Outline each blood parasite and name the species.
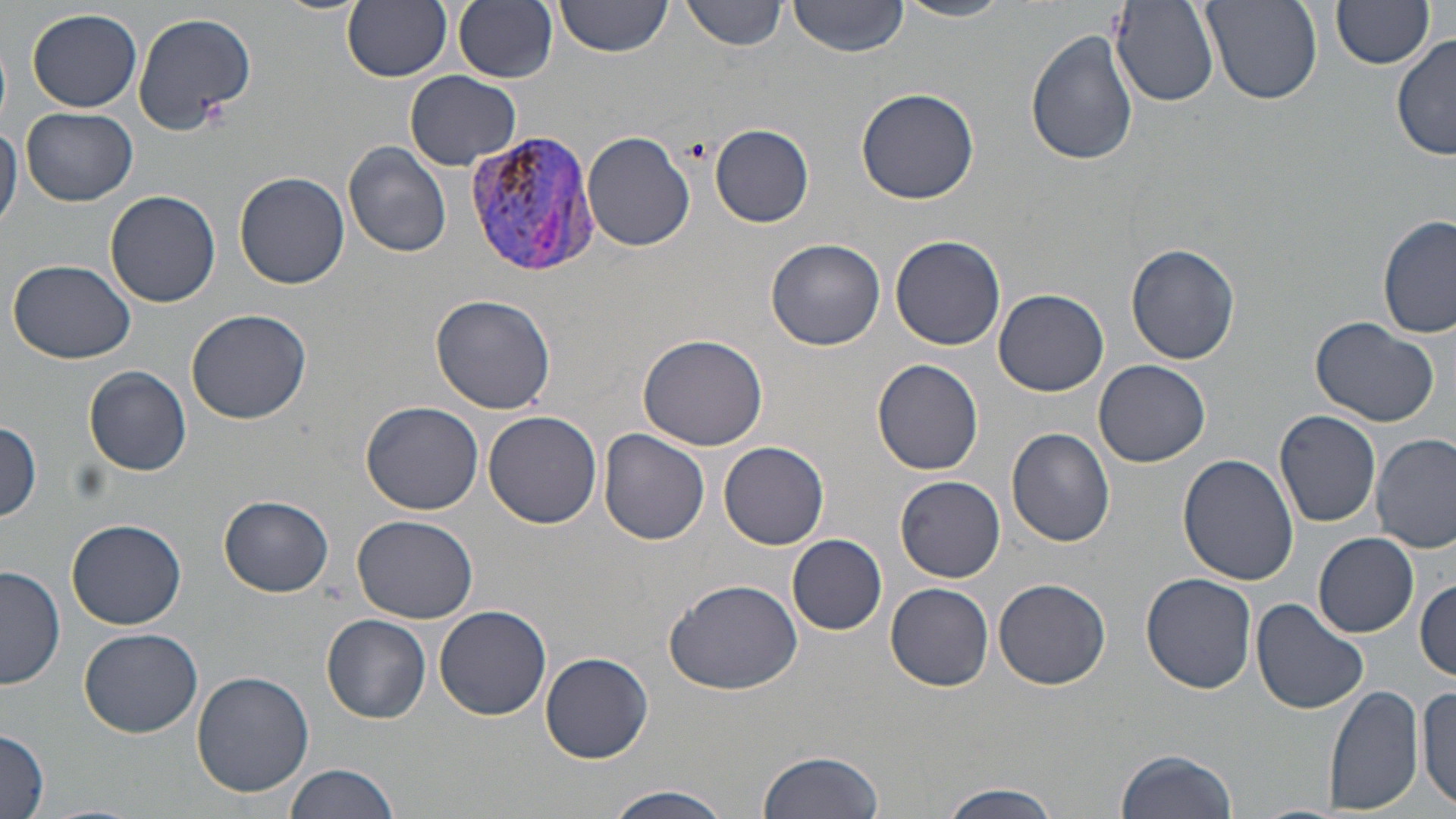

Approximate bounding boxes as (x1,y1)-(x2,y2) corner pairs in pixels.
Plasmodium vivax-infected red blood cells: (465,126)-(598,279).
No Plasmodium falciparum, Plasmodium ovale, Plasmodium malariae, Babesia divergens, or Trypanosoma brucei observed.

Uninfected red blood cell locations: (273,0)-(363,15), (342,0)-(453,82), (438,0)-(547,163), (453,0)-(559,82), (553,0)-(671,61), (682,0)-(790,52), (787,0)-(911,56), (896,0)-(1012,23), (1113,1)-(1221,107), (1201,1)-(1322,104), (1331,1)-(1434,70), (28,8)-(143,111), (130,9)-(259,136), (1026,29)-(1138,167), (1391,33)-(1455,160), (0,35)-(11,128), (405,72)-(524,172), (855,86)-(980,204), (21,108)-(141,206), (0,119)-(21,235), (711,124)-(814,228), (583,133)-(694,252), (343,142)-(453,258), (234,170)-(350,289), (105,190)-(221,308), (1377,215)-(1454,337), (890,236)-(1007,352), (766,238)-(885,350), (1127,246)-(1240,365), (8,258)-(137,365), (994,288)-(1109,396), (430,293)-(556,414), (186,309)-(312,424), (1309,317)-(1439,427), (637,333)-(769,451), (872,358)-(986,475), (1094,360)-(1212,468), (85,366)-(192,476), (360,400)-(486,514), (482,409)-(603,530), (1273,410)-(1383,528), (0,421)-(44,523), (597,428)-(711,545), (1006,428)-(1117,548), (1371,431)-(1455,553), (719,441)-(830,549), (1180,453)-(1298,585), (895,475)-(1006,583), (219,494)-(333,597), (352,514)-(476,623), (68,519)-(186,630), (787,533)-(887,635), (1314,533)-(1420,637), (0,563)-(66,692), (1141,572)-(1258,694), (665,575)-(805,696), (994,577)-(1111,690), (1415,579)-(1455,681), (886,582)-(994,691), (1251,598)-(1370,715), (434,606)-(552,721), (321,615)-(431,722), (79,627)-(204,737), (540,653)-(653,762), (192,670)-(314,797), (1324,684)-(1424,815), (1417,685)-(1455,813), (0,729)-(50,818), (1115,747)-(1237,819), (757,751)-(883,819), (284,763)-(398,819), (937,782)-(1062,819), (599,786)-(731,819). Slide-level diagnosis: Plasmodium vivax. Thin blood smear. Image is 1456×819 pixels. Optical microscopy. 1000x magnification. May-Grünwald-Giemsa-stained preparation. Single field of view.